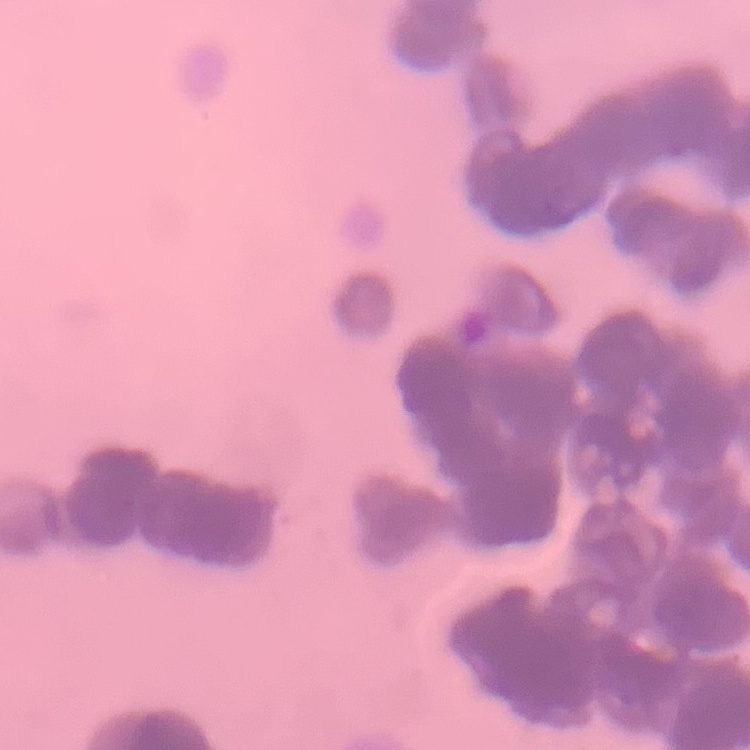
The red blood cells exhibit rouleaux formation. Field's or Giemsa stain. Thin blood smear. Square crop of a larger photomicrograph.